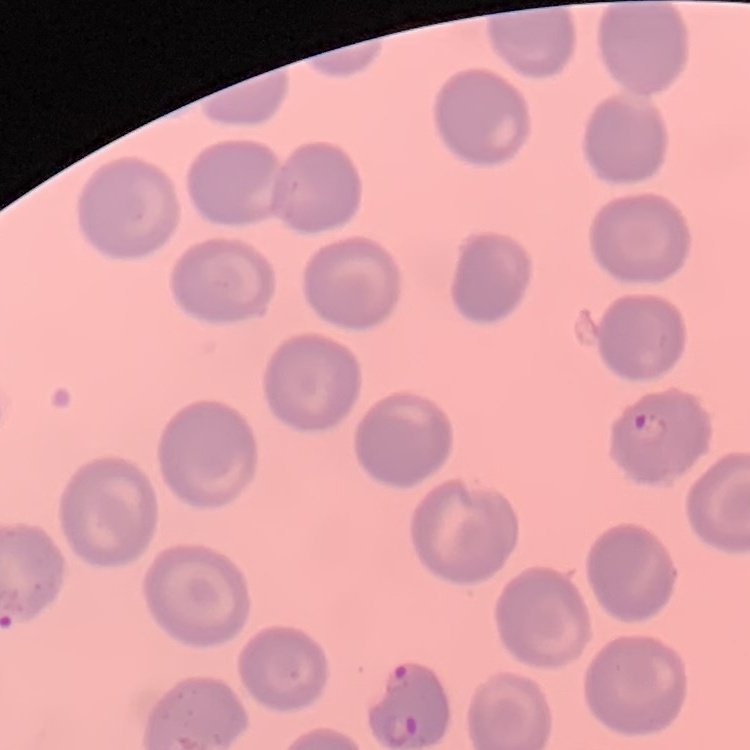

erythrocyte morphology = no rouleaux formation
preparation = thin peripheral smear
stain = Field's or Giemsa
image type = square crop of a larger photomicrograph